Comment on the morphology of the red blood cells.
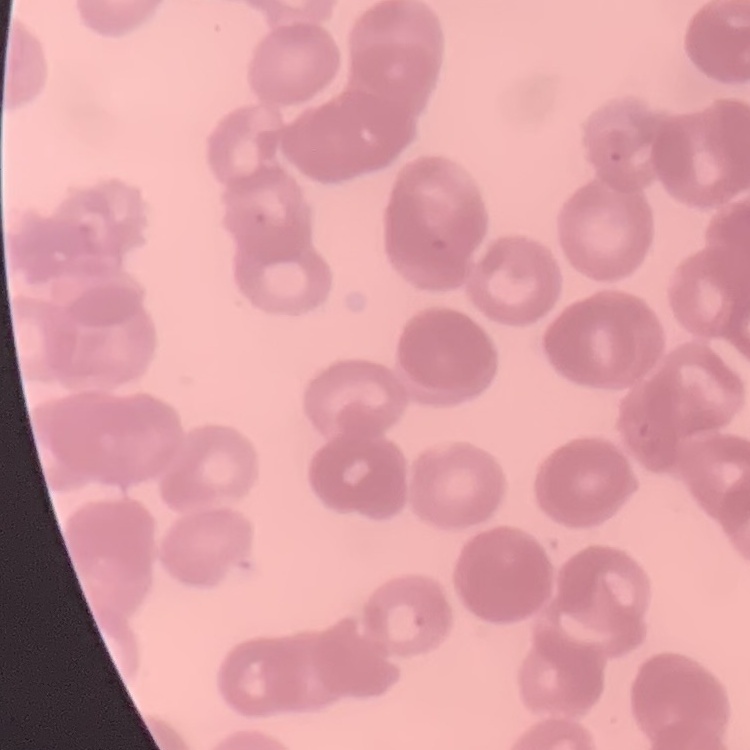
They show rouleaux formation.

Summary:
  - Image type: square crop of a larger photomicrograph
  - Preparation: thin peripheral smear
  - Stain: Field's or Giemsa